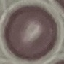
Summary:
  - Malaria status: uninfected
  - Capture: smartphone camera at the microscope eyepiece
  - Image type: automatically extracted cell patch, resized to 64 × 64 pixels
  - Stain: Giemsa
  - Preparation: thin smear